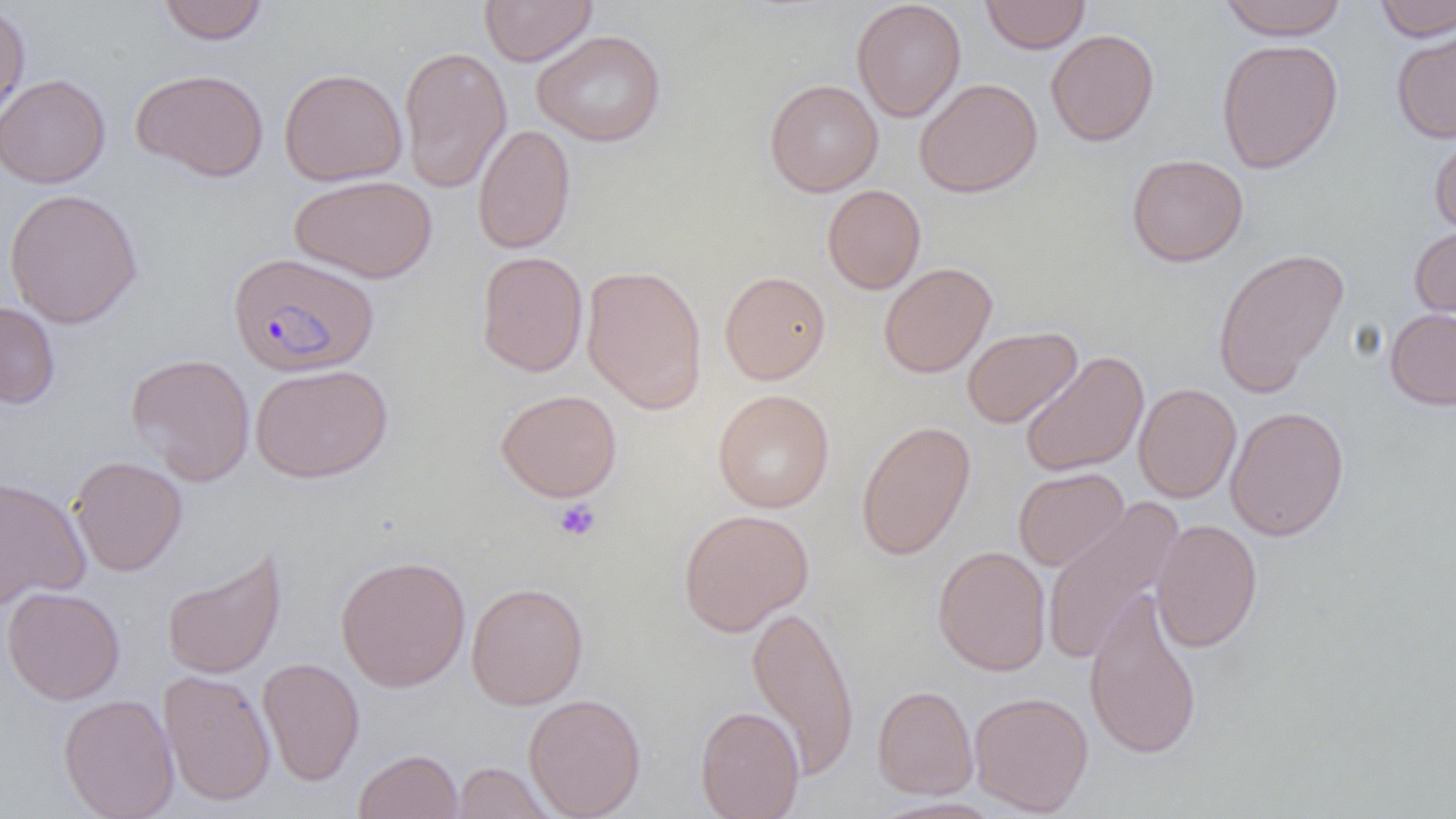

Summary:
  - Coordinate format: approximate bounding boxes as named x1/y1/x2/y2 corners in pixels
  - Plasmodium falciparum-infected red blood cell locations: (x1=227, y1=252, x2=379, y2=376)
  - Uninfected red blood cell locations: (x1=157, y1=0, x2=269, y2=45), (x1=479, y1=0, x2=597, y2=66), (x1=851, y1=0, x2=966, y2=122), (x1=981, y1=0, x2=1090, y2=53), (x1=1218, y1=0, x2=1348, y2=40), (x1=1374, y1=0, x2=1456, y2=41), (x1=0, y1=3, x2=30, y2=127), (x1=1046, y1=28, x2=1160, y2=146), (x1=1391, y1=28, x2=1456, y2=143), (x1=531, y1=29, x2=667, y2=147), (x1=1216, y1=38, x2=1344, y2=173), (x1=398, y1=46, x2=512, y2=192), (x1=131, y1=68, x2=269, y2=182), (x1=278, y1=68, x2=408, y2=186), (x1=0, y1=73, x2=110, y2=188), (x1=914, y1=78, x2=1042, y2=198), (x1=764, y1=79, x2=883, y2=196), (x1=473, y1=123, x2=576, y2=254), (x1=1428, y1=128, x2=1456, y2=238), (x1=1126, y1=154, x2=1249, y2=267), (x1=289, y1=175, x2=438, y2=283), (x1=822, y1=184, x2=926, y2=294), (x1=3, y1=188, x2=143, y2=328), (x1=1409, y1=224, x2=1456, y2=328), (x1=1212, y1=247, x2=1350, y2=398), (x1=476, y1=251, x2=588, y2=377), (x1=879, y1=262, x2=997, y2=378), (x1=581, y1=264, x2=707, y2=414), (x1=719, y1=270, x2=831, y2=384), (x1=0, y1=300, x2=60, y2=409), (x1=1385, y1=308, x2=1456, y2=410), (x1=962, y1=326, x2=1082, y2=428), (x1=1019, y1=351, x2=1149, y2=477), (x1=126, y1=353, x2=255, y2=485), (x1=250, y1=364, x2=393, y2=483), (x1=1133, y1=383, x2=1241, y2=503), (x1=495, y1=388, x2=622, y2=502), (x1=713, y1=389, x2=834, y2=513), (x1=1225, y1=406, x2=1350, y2=542), (x1=856, y1=420, x2=976, y2=561), (x1=69, y1=455, x2=187, y2=576), (x1=1013, y1=467, x2=1129, y2=571), (x1=0, y1=476, x2=90, y2=610), (x1=1041, y1=498, x2=1184, y2=666), (x1=678, y1=509, x2=814, y2=636), (x1=1151, y1=519, x2=1263, y2=653), (x1=932, y1=545, x2=1051, y2=676), (x1=161, y1=548, x2=287, y2=680), (x1=335, y1=554, x2=471, y2=692), (x1=466, y1=581, x2=588, y2=710), (x1=2, y1=586, x2=125, y2=705), (x1=1083, y1=589, x2=1203, y2=760), (x1=747, y1=604, x2=860, y2=779), (x1=257, y1=657, x2=365, y2=786), (x1=159, y1=669, x2=276, y2=807), (x1=872, y1=685, x2=978, y2=799), (x1=969, y1=691, x2=1094, y2=816), (x1=58, y1=693, x2=179, y2=819), (x1=523, y1=693, x2=646, y2=818), (x1=695, y1=706, x2=805, y2=819), (x1=353, y1=749, x2=463, y2=819), (x1=450, y1=761, x2=555, y2=819)
  - Platelet locations: (x1=554, y1=498, x2=601, y2=541)
  - Slide-level diagnosis: Plasmodium falciparum
  - Magnification: 1000x
  - Field of view: one of a larger specimen
  - Modality: light microscopy
  - Image size: 1456×819 pixels
  - Preparation: thin blood smear